Classify this cell by malaria status.
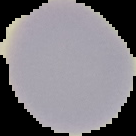
It is uninfected.

Summary:
  - Preparation: thin blood film
  - Image type: segmented cell region with the area outside set to black
  - Image size: 136×136 pixels